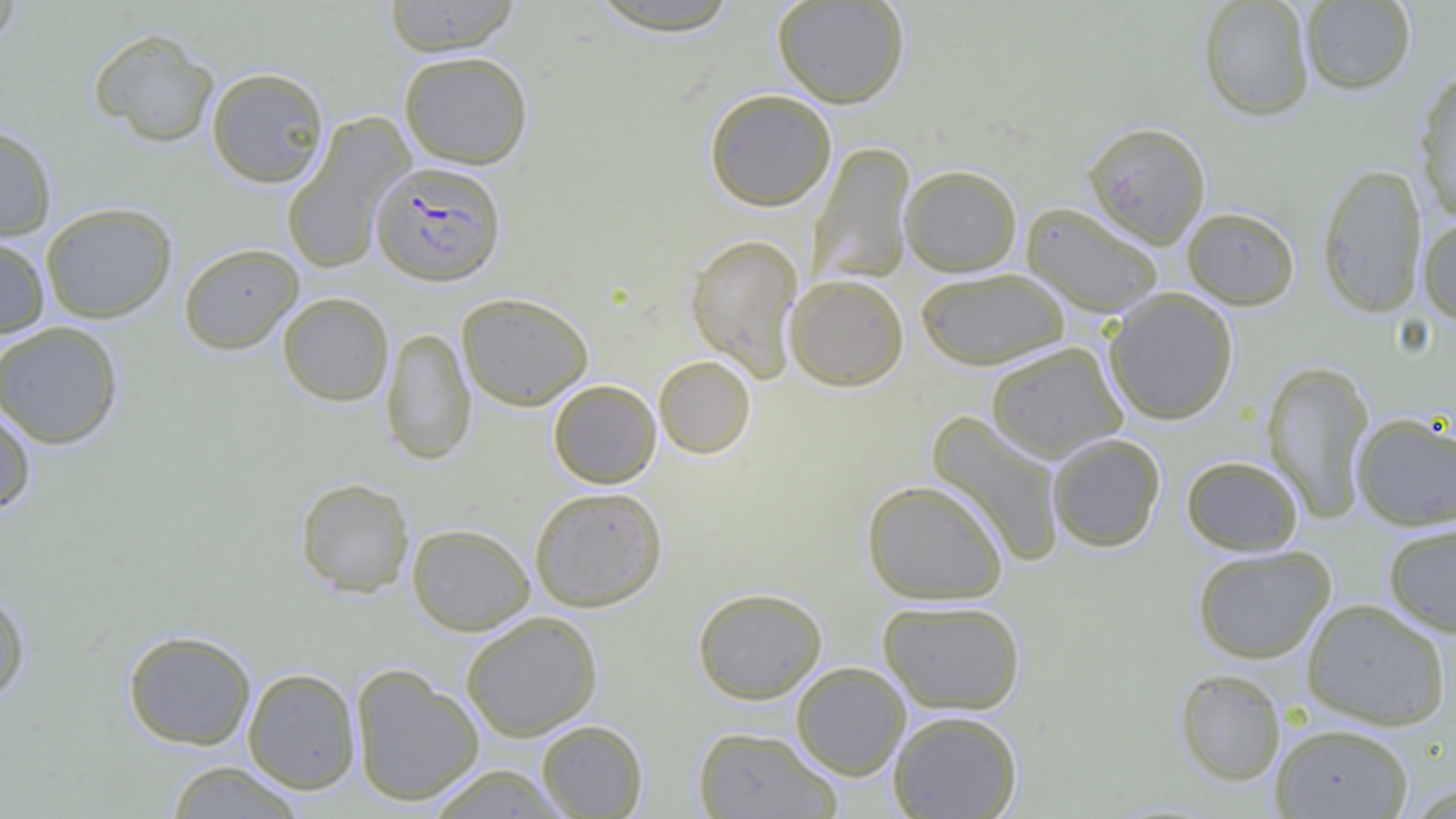

Approximate bounding boxes as named x1/y1/x2/y2 corners in pixels. Uninfected red blood cell locations: (x1=0, y1=0, x2=24, y2=52), (x1=382, y1=0, x2=522, y2=56), (x1=772, y1=0, x2=910, y2=108), (x1=1198, y1=0, x2=1315, y2=120), (x1=584, y1=1, x2=747, y2=36), (x1=1301, y1=1, x2=1416, y2=94), (x1=88, y1=27, x2=220, y2=147), (x1=398, y1=50, x2=534, y2=169), (x1=206, y1=66, x2=330, y2=187), (x1=1414, y1=67, x2=1456, y2=221), (x1=703, y1=88, x2=837, y2=211), (x1=281, y1=114, x2=414, y2=274), (x1=1082, y1=120, x2=1211, y2=248), (x1=0, y1=123, x2=58, y2=241), (x1=810, y1=142, x2=916, y2=285), (x1=1316, y1=162, x2=1428, y2=318), (x1=899, y1=164, x2=1023, y2=276), (x1=40, y1=202, x2=177, y2=323), (x1=1022, y1=202, x2=1165, y2=319), (x1=1182, y1=206, x2=1300, y2=310), (x1=1417, y1=215, x2=1456, y2=324), (x1=0, y1=233, x2=50, y2=339), (x1=685, y1=233, x2=804, y2=381), (x1=178, y1=242, x2=304, y2=354), (x1=915, y1=267, x2=1071, y2=371), (x1=784, y1=273, x2=909, y2=391), (x1=1103, y1=288, x2=1239, y2=425), (x1=277, y1=292, x2=394, y2=406), (x1=457, y1=292, x2=594, y2=411), (x1=0, y1=321, x2=125, y2=449), (x1=381, y1=327, x2=476, y2=465), (x1=985, y1=341, x2=1128, y2=463), (x1=653, y1=355, x2=756, y2=459), (x1=1262, y1=360, x2=1376, y2=522), (x1=548, y1=379, x2=662, y2=488), (x1=0, y1=403, x2=36, y2=516), (x1=927, y1=411, x2=1067, y2=566), (x1=1352, y1=411, x2=1456, y2=530), (x1=1047, y1=432, x2=1166, y2=552), (x1=1180, y1=454, x2=1303, y2=556), (x1=294, y1=477, x2=416, y2=598), (x1=861, y1=478, x2=1010, y2=605), (x1=529, y1=486, x2=668, y2=612), (x1=1383, y1=521, x2=1456, y2=637), (x1=406, y1=523, x2=535, y2=635), (x1=1191, y1=545, x2=1336, y2=664), (x1=0, y1=586, x2=31, y2=707), (x1=692, y1=587, x2=828, y2=704), (x1=1301, y1=598, x2=1451, y2=730), (x1=877, y1=599, x2=1026, y2=715), (x1=461, y1=611, x2=603, y2=741), (x1=122, y1=628, x2=257, y2=750), (x1=790, y1=662, x2=911, y2=781), (x1=350, y1=665, x2=485, y2=807), (x1=242, y1=667, x2=361, y2=794), (x1=1174, y1=668, x2=1286, y2=786), (x1=887, y1=709, x2=1023, y2=819), (x1=535, y1=719, x2=648, y2=818), (x1=1270, y1=723, x2=1414, y2=819), (x1=692, y1=726, x2=842, y2=818), (x1=164, y1=760, x2=307, y2=818), (x1=422, y1=764, x2=573, y2=818). Plasmodium falciparum-infected red blood cell locations: (x1=370, y1=160, x2=506, y2=286). Slide-level diagnosis: Plasmodium falciparum. Thin blood film. Captured at 1000x magnification. Image is 1456×819 pixels. Light microscopy. One field of a larger specimen.